Report the malaria status of this cell.
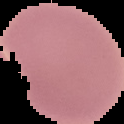
It is uninfected.

{
  "image_type": "segmented cell region with the area outside set to black",
  "image_size": "124×124 pixels",
  "preparation": "thin blood smear"
}